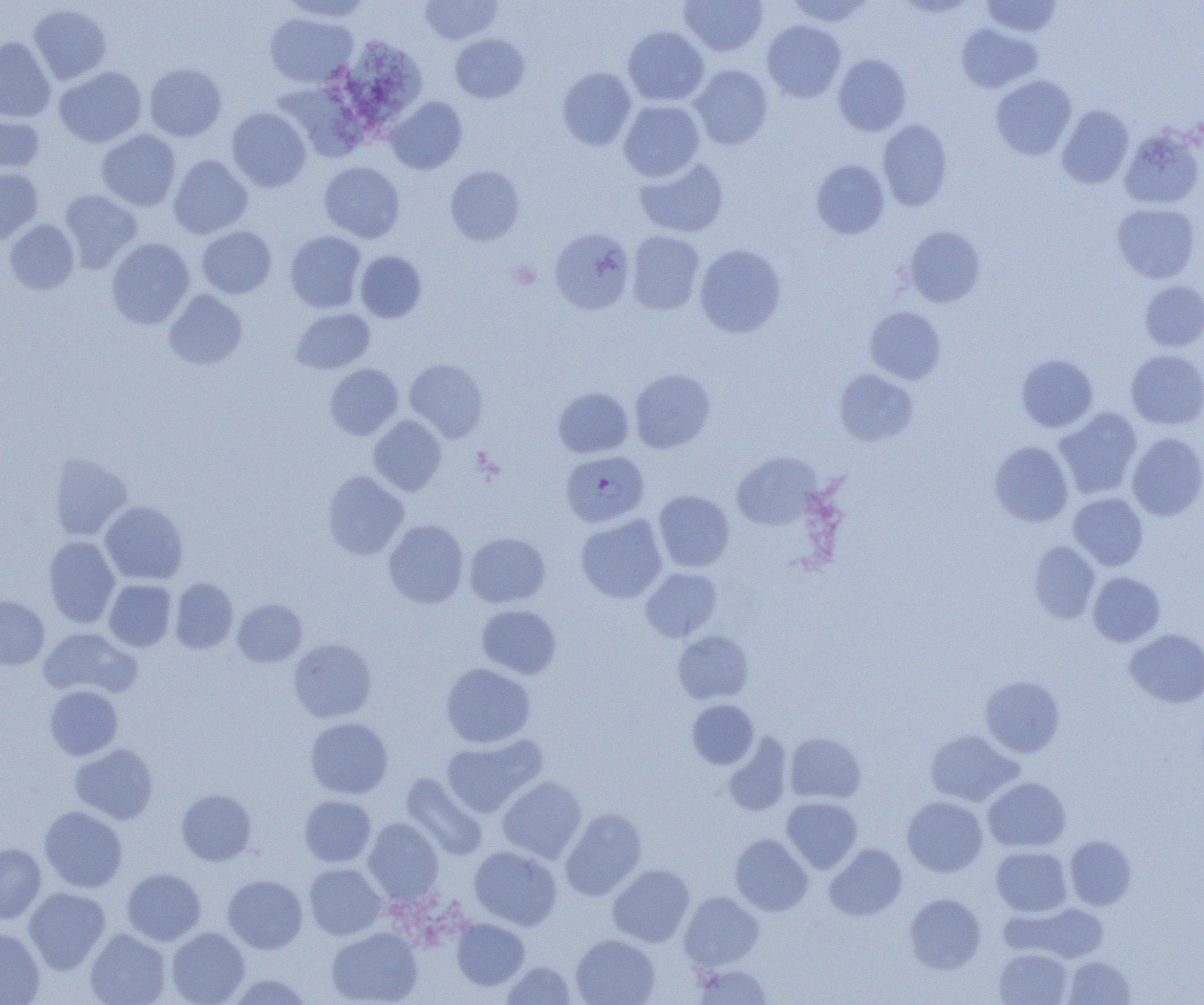

slide-level diagnosis = Plasmodium falciparum
preparation = thin blood film
magnification = 1000x
modality = light microscopy
image size = 1204×1005 pixels
field of view = single
uninfected red blood cell locations = approximate bounding boxes as (x1, y1, x2, y2) in pixels: (280, 0, 374, 22), (419, 0, 502, 44), (680, 0, 768, 56), (785, 0, 874, 27), (981, 0, 1064, 37), (894, 1, 979, 18), (28, 4, 111, 84), (265, 12, 357, 88), (762, 20, 845, 102), (956, 23, 1043, 93), (623, 26, 709, 105), (450, 34, 529, 102), (0, 37, 55, 122), (353, 37, 429, 125), (833, 54, 911, 135), (144, 64, 227, 141), (689, 64, 773, 149), (54, 67, 146, 147), (557, 67, 637, 150), (991, 74, 1076, 160), (277, 83, 377, 162), (386, 96, 467, 174), (618, 100, 705, 181), (1057, 105, 1134, 188), (227, 107, 311, 191), (0, 110, 44, 175), (878, 119, 953, 210), (1120, 128, 1204, 209), (96, 130, 180, 211), (169, 154, 253, 239), (634, 157, 729, 238), (811, 159, 890, 239), (320, 162, 404, 243), (445, 165, 524, 246), (0, 167, 43, 245), (59, 189, 142, 272), (1112, 202, 1201, 283), (4, 219, 79, 294), (903, 225, 986, 308), (197, 226, 276, 299), (549, 228, 635, 315), (285, 231, 366, 313), (626, 231, 705, 315), (106, 238, 195, 329), (694, 244, 786, 338), (355, 251, 426, 322), (1140, 280, 1204, 351), (164, 289, 247, 369), (864, 306, 947, 384), (291, 308, 374, 374), (1125, 349, 1204, 429), (1017, 354, 1098, 431), (405, 358, 489, 441), (325, 363, 403, 439), (629, 368, 716, 453), (833, 368, 919, 446), (553, 387, 634, 458), (1054, 407, 1142, 499), (368, 415, 447, 496), (1127, 432, 1204, 520), (989, 441, 1073, 526), (48, 452, 132, 540), (731, 452, 820, 530), (323, 471, 408, 560), (653, 490, 734, 572), (1069, 493, 1148, 570), (100, 501, 188, 584), (575, 514, 667, 603), (384, 519, 468, 608), (465, 532, 550, 607), (43, 536, 120, 627), (1029, 541, 1100, 624), (641, 567, 722, 642), (1088, 572, 1166, 646), (170, 577, 238, 654), (104, 579, 176, 651), (0, 597, 49, 670), (233, 599, 307, 667), (476, 605, 561, 678), (39, 627, 141, 699), (1125, 629, 1204, 708), (673, 630, 754, 704), (288, 638, 377, 723), (441, 663, 536, 748), (980, 676, 1065, 757), (45, 685, 123, 759), (687, 699, 759, 769), (305, 717, 393, 798), (925, 729, 1022, 806), (785, 732, 866, 804), (441, 734, 546, 817), (724, 734, 793, 816), (70, 743, 158, 824), (401, 773, 488, 861), (497, 776, 586, 862), (983, 776, 1071, 852), (177, 789, 256, 865), (299, 796, 376, 867), (902, 796, 988, 877), (781, 797, 862, 873), (39, 806, 127, 892), (560, 808, 646, 901), (362, 817, 443, 903), (730, 834, 813, 916), (1064, 835, 1137, 910), (0, 843, 46, 923), (825, 843, 907, 920), (469, 846, 562, 930), (991, 847, 1073, 916), (304, 863, 386, 939), (607, 864, 695, 947), (122, 868, 206, 945), (223, 875, 308, 953), (23, 887, 111, 974), (680, 891, 763, 971), (905, 893, 986, 974), (1008, 902, 1109, 963), (451, 918, 529, 989), (0, 927, 45, 1004), (167, 927, 249, 1005), (326, 927, 422, 1005), (85, 928, 170, 1005), (571, 935, 659, 1005), (994, 948, 1072, 1005), (1064, 956, 1135, 1004), (502, 961, 576, 1005), (693, 964, 774, 1004), (224, 974, 314, 1004)
Plasmodium falciparum-infected red blood cell locations = approximate bounding boxes as (x1, y1, x2, y2) in pixels: (561, 450, 649, 527)